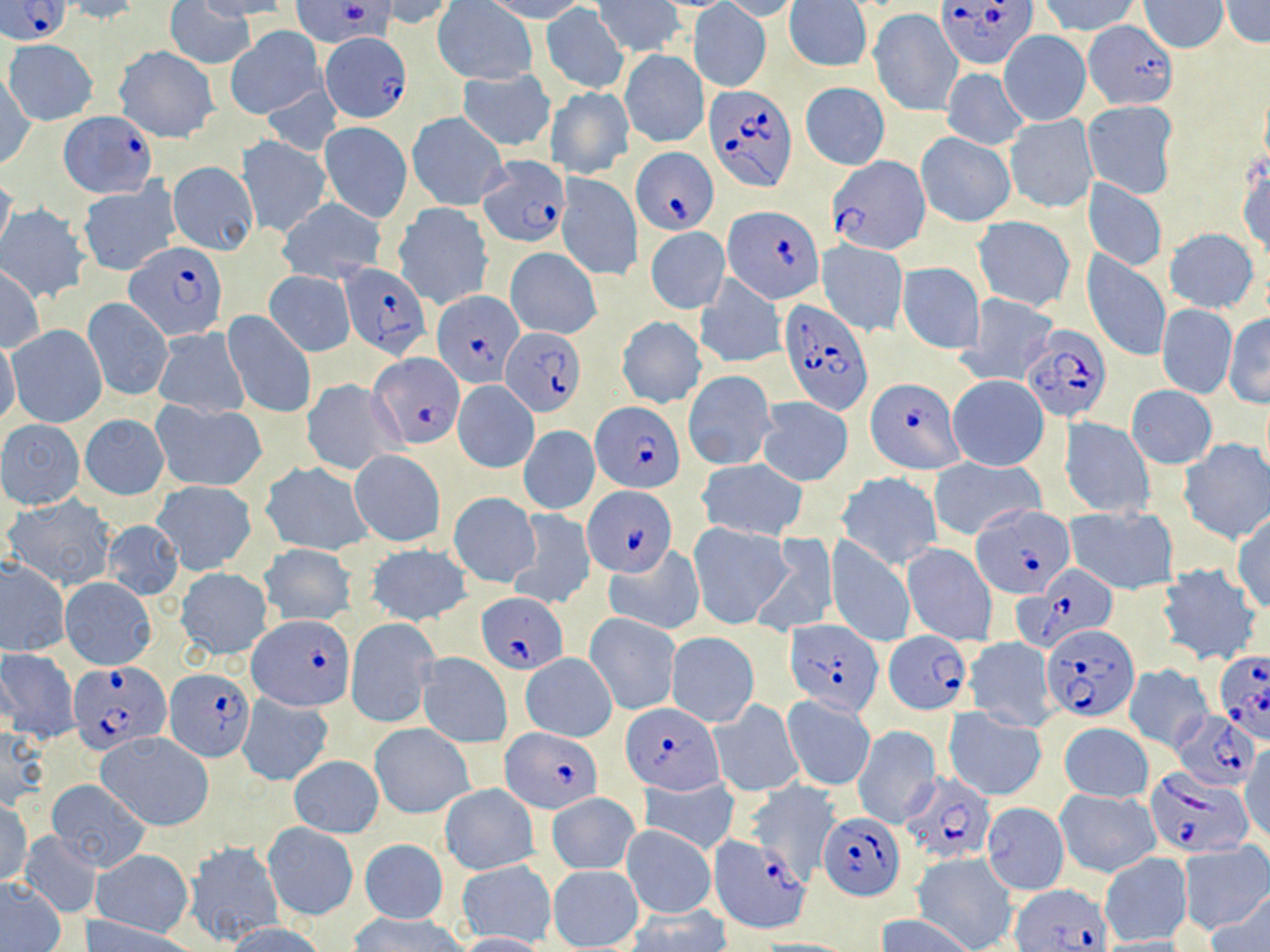
{
  "plasmodium_falciparum_infected_red_blood_cell_locations": "approximate bounding boxes as (x1, y1, x2, y2) in pixels: (0, 0, 73, 46), (290, 0, 395, 47), (937, 0, 1038, 71), (321, 34, 411, 122), (702, 83, 796, 190), (59, 112, 156, 197), (633, 148, 720, 234), (476, 155, 571, 248), (828, 156, 929, 258), (723, 204, 822, 305), (128, 245, 229, 341), (339, 263, 431, 359), (431, 292, 522, 388), (779, 299, 875, 415), (1021, 323, 1113, 423), (501, 327, 586, 415), (370, 353, 465, 448), (867, 379, 963, 474), (590, 402, 685, 493), (583, 484, 677, 578), (971, 503, 1072, 597), (1021, 564, 1115, 649), (478, 592, 568, 674), (249, 613, 352, 710), (785, 618, 881, 715), (1042, 624, 1138, 721), (884, 631, 971, 716), (1213, 651, 1270, 741), (70, 662, 171, 756), (165, 666, 255, 761), (623, 705, 723, 793), (1173, 709, 1259, 790), (503, 729, 601, 811), (1146, 768, 1251, 859), (898, 770, 997, 865), (819, 813, 905, 900), (709, 826, 814, 934), (1010, 885, 1114, 951)",
  "slide_level_diagnosis": "Plasmodium falciparum",
  "image_size": "1270×952 pixels",
  "uninfected_red_blood_cell_locations": "approximate bounding boxes as (x1, y1, x2, y2) in pixels: (163, 0, 254, 70), (195, 0, 294, 20), (482, 0, 588, 23), (719, 0, 803, 20), (1037, 0, 1142, 37), (1219, 0, 1270, 48), (59, 1, 144, 25), (375, 1, 460, 29), (435, 1, 537, 86), (594, 1, 683, 57), (786, 1, 871, 71), (1137, 1, 1228, 53), (691, 3, 771, 91), (541, 5, 629, 94), (867, 9, 961, 116), (1085, 20, 1178, 110), (227, 26, 325, 119), (998, 31, 1090, 125), (4, 39, 97, 125), (115, 46, 219, 143), (620, 50, 709, 148), (942, 67, 1029, 150), (457, 69, 556, 152), (2, 71, 36, 171), (262, 82, 340, 157), (800, 82, 889, 170), (543, 86, 633, 179), (1083, 101, 1177, 197), (407, 112, 508, 209), (1006, 115, 1096, 211), (319, 121, 412, 223), (916, 132, 1015, 227), (236, 135, 331, 238), (1237, 151, 1269, 260), (166, 161, 258, 255), (556, 172, 641, 283), (0, 174, 17, 255), (76, 179, 180, 276), (1084, 180, 1169, 271), (278, 198, 386, 283), (393, 203, 494, 311), (1, 205, 90, 302), (972, 215, 1076, 312), (645, 226, 729, 314), (1164, 228, 1260, 313), (817, 240, 908, 335), (505, 247, 602, 341), (1082, 249, 1172, 363), (897, 261, 985, 354), (0, 265, 43, 353), (265, 271, 356, 357), (693, 274, 785, 370), (956, 292, 1061, 387), (82, 297, 173, 401), (1156, 304, 1235, 398), (222, 310, 317, 419), (1224, 313, 1270, 408), (617, 317, 705, 410), (8, 325, 107, 428), (151, 327, 250, 416), (0, 338, 21, 428), (683, 370, 776, 469), (947, 374, 1049, 472), (300, 378, 402, 476), (452, 380, 540, 473), (1126, 385, 1217, 469), (757, 398, 854, 486), (153, 400, 268, 491), (79, 414, 169, 500), (1060, 416, 1154, 518), (0, 420, 84, 510), (518, 425, 600, 515), (1179, 438, 1270, 545), (349, 449, 445, 547), (929, 456, 1044, 539), (698, 459, 809, 541), (263, 464, 375, 554), (835, 471, 943, 570), (153, 481, 257, 576), (448, 492, 541, 587), (4, 496, 119, 589), (1065, 506, 1181, 596), (509, 509, 596, 611), (1232, 514, 1270, 613), (102, 518, 183, 602), (688, 523, 792, 629), (750, 533, 838, 638), (825, 537, 916, 648), (901, 542, 999, 646), (258, 543, 356, 628), (363, 544, 472, 627), (604, 544, 706, 635), (0, 559, 70, 656), (1156, 563, 1263, 666), (174, 568, 273, 661), (60, 577, 156, 670), (584, 613, 681, 714), (346, 618, 440, 728), (666, 632, 760, 726), (963, 638, 1058, 732), (0, 649, 79, 743), (417, 652, 512, 746), (521, 653, 616, 742), (1122, 663, 1213, 752), (236, 693, 334, 786), (782, 695, 876, 790), (709, 700, 804, 797), (945, 708, 1047, 800), (1059, 722, 1153, 802), (1, 723, 51, 810), (369, 723, 473, 818), (852, 726, 942, 828), (96, 734, 213, 832), (1241, 740, 1269, 841), (288, 755, 383, 836), (639, 776, 741, 857), (46, 779, 151, 872), (748, 782, 841, 884), (439, 784, 539, 874), (1054, 788, 1161, 877), (545, 792, 640, 875), (0, 800, 32, 887), (981, 802, 1069, 896), (262, 823, 359, 922), (620, 825, 716, 919), (212, 826, 334, 935), (18, 833, 103, 919), (358, 839, 448, 925), (184, 840, 285, 945), (1179, 842, 1270, 936), (92, 848, 192, 936), (911, 852, 1018, 952), (1099, 852, 1191, 946), (457, 859, 557, 947), (546, 864, 645, 949), (1, 877, 65, 950), (1204, 892, 1270, 951), (624, 907, 732, 952), (350, 913, 470, 952), (878, 914, 976, 952), (84, 919, 195, 952), (223, 923, 328, 952), (455, 931, 549, 952), (748, 937, 861, 951)",
  "field_of_view": "single",
  "magnification": "1000x",
  "modality": "light microscopy",
  "stain": "May-Grünwald-Giemsa",
  "preparation": "thin blood smear"
}